State the blood parasite species.
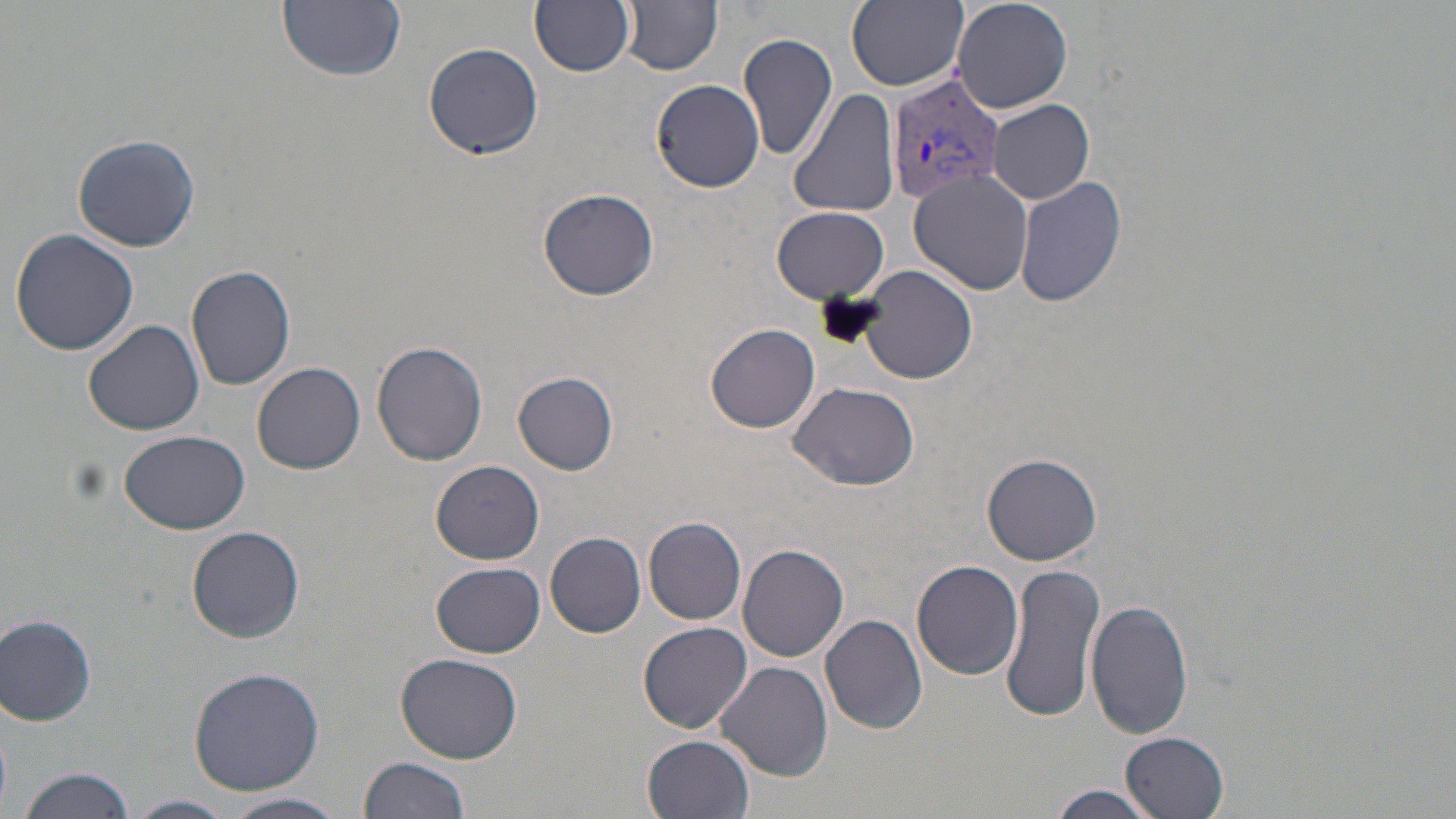

Plasmodium vivax.

Approximate bounding boxes as named x1/y1/x2/y2 corners in pixels. Plasmodium vivax-infected red blood cell locations: (x1=887, y1=73, x2=1006, y2=207). Uninfected red blood cell locations: (x1=277, y1=0, x2=406, y2=81), (x1=530, y1=0, x2=636, y2=76), (x1=846, y1=0, x2=968, y2=95), (x1=953, y1=0, x2=1074, y2=113), (x1=621, y1=1, x2=723, y2=74), (x1=739, y1=32, x2=838, y2=161), (x1=422, y1=41, x2=545, y2=160), (x1=652, y1=79, x2=765, y2=192), (x1=789, y1=89, x2=901, y2=220), (x1=988, y1=100, x2=1096, y2=204), (x1=73, y1=133, x2=200, y2=252), (x1=909, y1=171, x2=1033, y2=296), (x1=1012, y1=175, x2=1129, y2=309), (x1=539, y1=187, x2=659, y2=300), (x1=773, y1=206, x2=889, y2=302), (x1=9, y1=228, x2=142, y2=356), (x1=186, y1=265, x2=297, y2=391), (x1=858, y1=265, x2=978, y2=385), (x1=82, y1=318, x2=206, y2=437), (x1=707, y1=323, x2=822, y2=434), (x1=371, y1=340, x2=488, y2=466), (x1=252, y1=361, x2=367, y2=474), (x1=513, y1=371, x2=620, y2=474), (x1=789, y1=381, x2=919, y2=491), (x1=118, y1=430, x2=251, y2=534), (x1=983, y1=452, x2=1101, y2=565), (x1=430, y1=459, x2=544, y2=565), (x1=643, y1=515, x2=748, y2=625), (x1=187, y1=525, x2=306, y2=643), (x1=545, y1=532, x2=647, y2=638), (x1=737, y1=544, x2=848, y2=662), (x1=914, y1=560, x2=1024, y2=680), (x1=999, y1=561, x2=1106, y2=724), (x1=431, y1=563, x2=545, y2=657), (x1=1086, y1=599, x2=1193, y2=740), (x1=821, y1=613, x2=928, y2=735), (x1=2, y1=614, x2=97, y2=726), (x1=638, y1=621, x2=753, y2=733), (x1=396, y1=651, x2=524, y2=763), (x1=716, y1=661, x2=833, y2=783), (x1=187, y1=666, x2=326, y2=795), (x1=1120, y1=731, x2=1229, y2=817), (x1=643, y1=734, x2=753, y2=818), (x1=356, y1=756, x2=471, y2=819), (x1=17, y1=766, x2=136, y2=819), (x1=1041, y1=786, x2=1168, y2=817), (x1=221, y1=792, x2=350, y2=819), (x1=125, y1=794, x2=235, y2=819). 1000x magnification. Thin blood film. One field of a larger specimen. Optical microscopy. Image is 1456×819 pixels. May-Grünwald-Giemsa-stained preparation.